Report the malaria status.
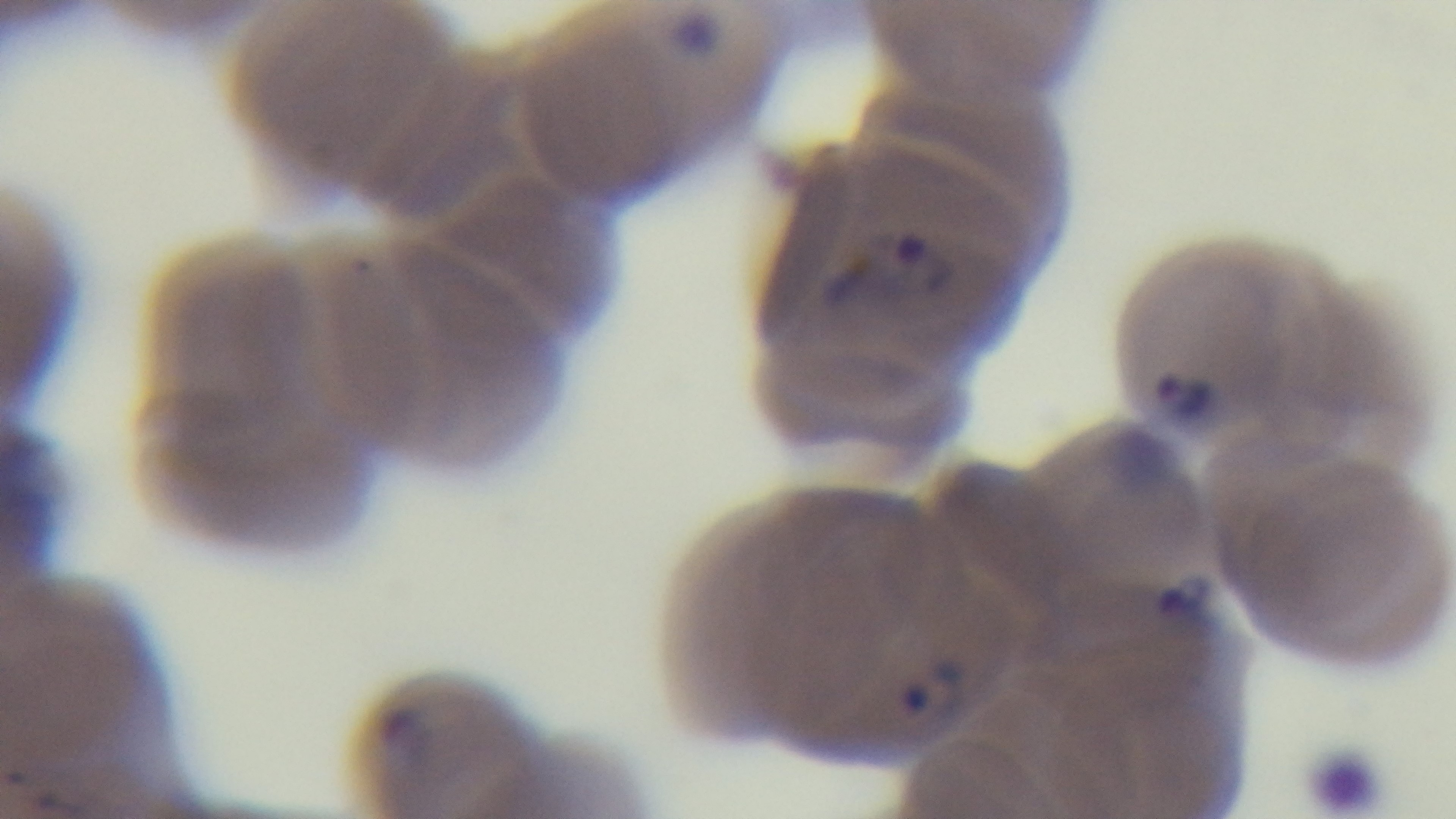
Positive.

stain = Giemsa
modality = light microscopy
capture = mounted 4K digital camera
preparation = thin
objective = 100x oil immersion
field of view = single